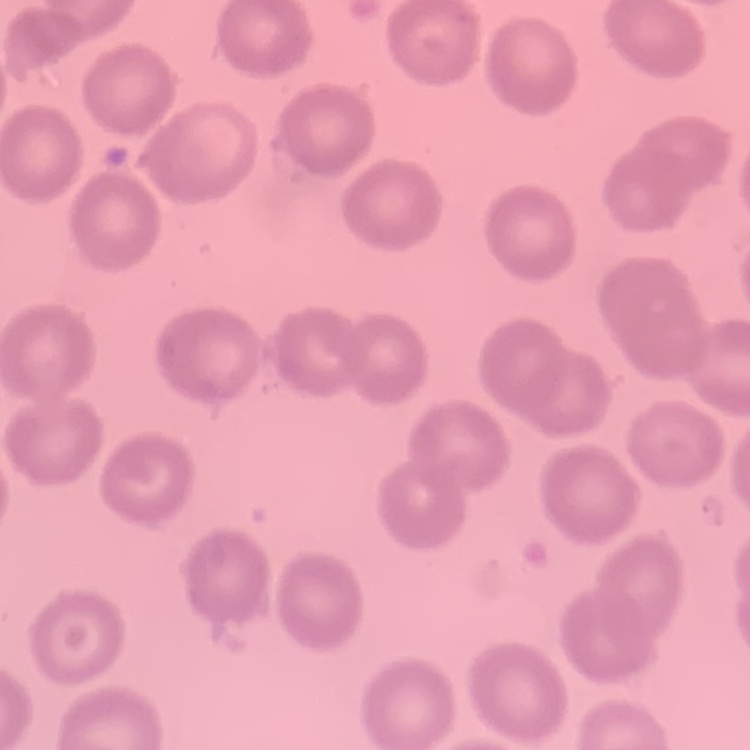
Summary:
  - Erythrocyte morphology: no rouleaux formation
  - Stain: Field's or Giemsa
  - Image type: one tile cut from a larger photomicrograph
  - Preparation: thin blood film